Give the position of every Plasmodium parasite.
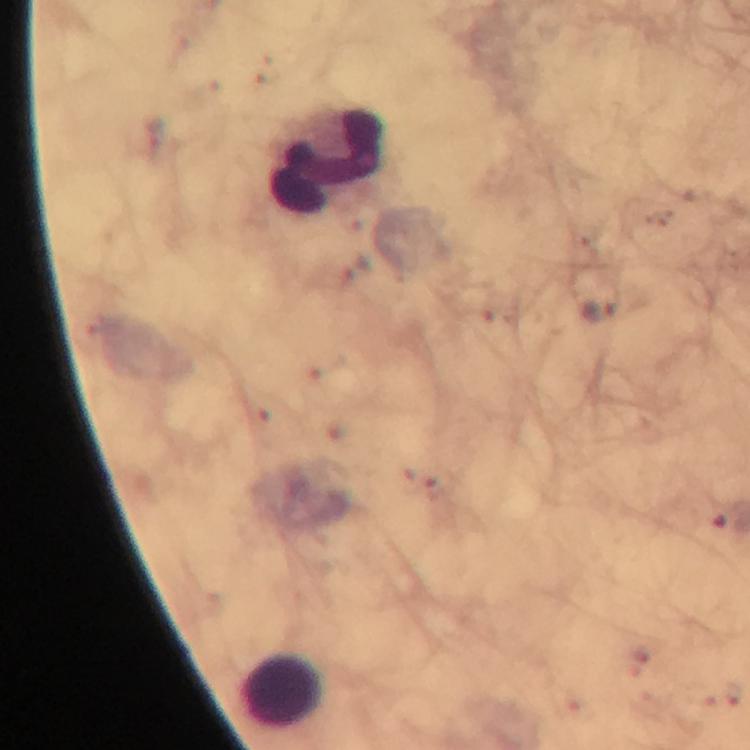
Approximate centers as {x, y} in pixels.
Plasmodium parasites: {599, 310}.

leukocyte_locations: 'approximate centers as {x, y} in pixels: {324, 159}, {283, 692}'
image_size: 750×750 pixels
magnification: 100x
immersion_oil: applied
context: from a diagnostic examination for malaria
preparation: thick blood film
capture: smartphone camera through the microscope
stain: Giemsa
cropped_from: one field of view